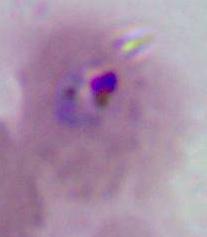

Photomicrograph. A Plasmodium parasite is seen. Captured at either 400x or 1000x magnification.